Locate and identify every blood parasite.
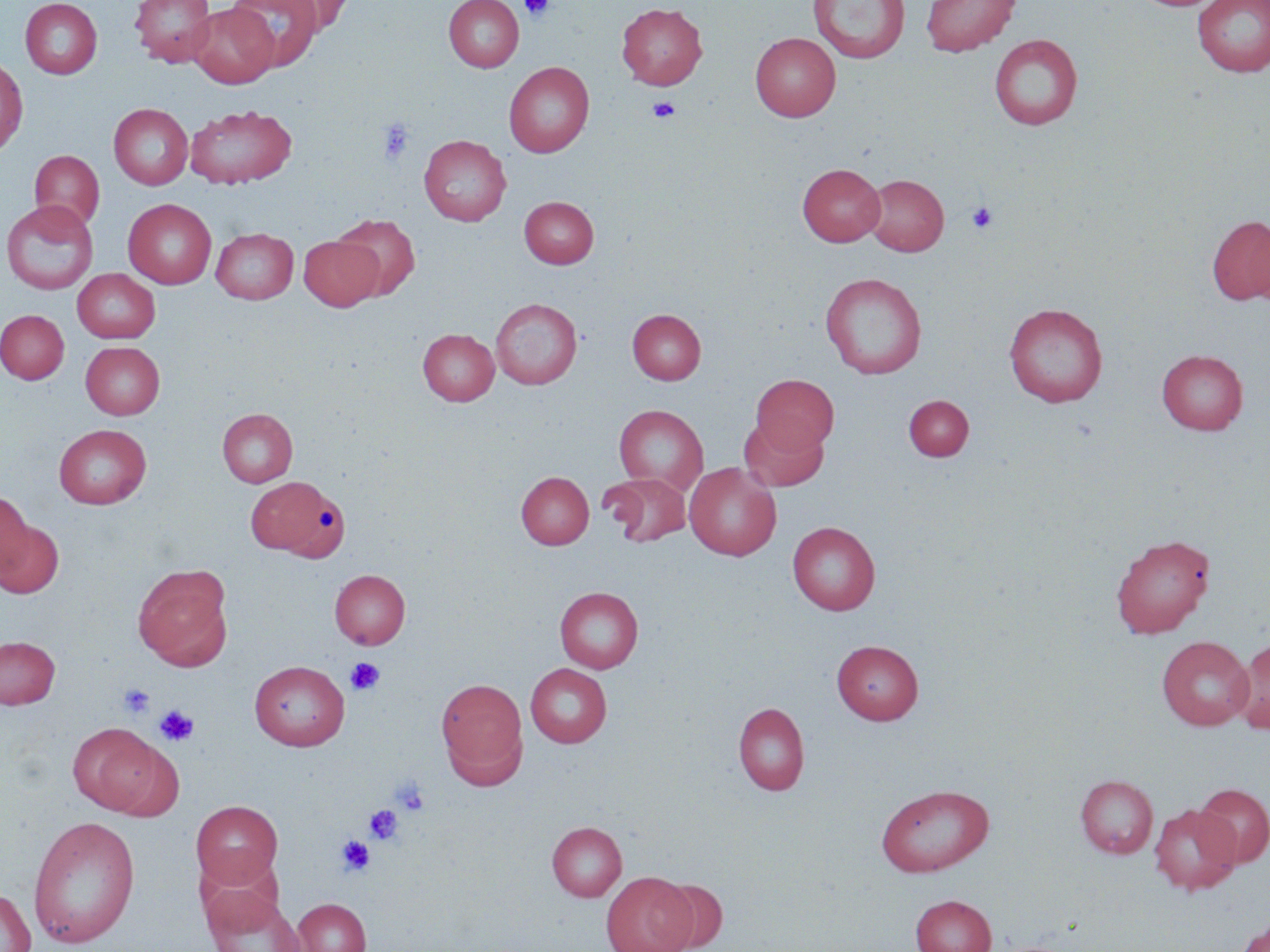
No blood parasites seen.

Approximate bounding boxes as (x1, y1, x2, y2) in pixels. Uninfected red blood cell locations: (20, 0, 102, 79), (130, 0, 217, 66), (228, 0, 323, 70), (271, 0, 355, 35), (443, 0, 524, 71), (809, 0, 908, 64), (920, 0, 1020, 56), (1193, 0, 1270, 78), (186, 3, 279, 88), (616, 3, 708, 90), (750, 32, 840, 121), (989, 33, 1083, 131), (0, 56, 28, 156), (503, 62, 594, 157), (108, 103, 193, 190), (185, 104, 297, 189), (419, 134, 511, 226), (29, 150, 105, 231), (797, 163, 885, 246), (864, 173, 949, 256), (520, 196, 598, 268), (123, 199, 217, 289), (1, 200, 99, 294), (332, 214, 421, 300), (1207, 215, 1270, 305), (1250, 220, 1270, 307), (211, 228, 298, 304), (298, 235, 383, 311), (73, 269, 160, 342), (820, 272, 928, 379), (490, 298, 582, 389), (1004, 302, 1108, 407), (0, 309, 69, 384), (627, 309, 706, 384), (418, 328, 499, 405), (81, 341, 165, 419), (1157, 349, 1248, 434), (751, 374, 839, 455), (903, 395, 973, 461), (614, 404, 708, 493), (217, 408, 298, 487), (739, 416, 828, 491), (53, 424, 152, 509), (684, 462, 781, 560), (516, 471, 594, 549), (603, 472, 691, 548), (246, 475, 349, 561), (0, 489, 33, 582), (0, 519, 63, 599), (788, 521, 880, 614), (1110, 533, 1215, 639), (133, 564, 234, 671), (330, 569, 410, 649), (555, 586, 643, 673), (0, 635, 60, 709), (1156, 635, 1254, 729), (1231, 638, 1270, 734), (832, 640, 923, 724), (249, 660, 350, 750), (525, 663, 612, 747), (435, 677, 528, 786), (733, 702, 809, 795), (68, 723, 174, 816), (1075, 774, 1158, 858), (875, 783, 994, 877), (1195, 783, 1270, 867), (191, 800, 282, 889), (1149, 803, 1242, 894), (27, 815, 141, 949), (547, 821, 627, 901), (195, 855, 287, 935), (601, 871, 697, 952), (655, 878, 728, 951), (203, 886, 307, 952), (0, 887, 35, 952), (911, 894, 995, 952), (293, 898, 372, 952), (1234, 916, 1270, 952). Platelet locations: (521, 0, 555, 22), (647, 97, 681, 122), (377, 119, 415, 165), (967, 202, 998, 233), (345, 657, 386, 696), (118, 683, 154, 718), (154, 706, 198, 746), (392, 777, 430, 816), (365, 804, 403, 845), (336, 835, 374, 876). Slide-level diagnosis: no evidence of blood parasites. Optical microscopy. Captured at 1000x magnification. Image is 1270×952 pixels. May-Grünwald-Giemsa stain. Single field of view. Thin blood smear.